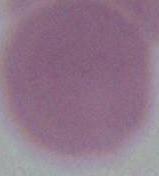
An erythrocyte is seen. Micrograph. 1000x magnification.